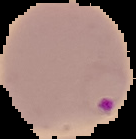

Summary:
  - Image type: segmented cell region on a black background
  - Result: malaria parasites detected
  - Preparation: thin blood film
  - Image size: 136×139 pixels